State which cell type is depicted.
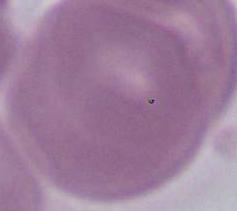
This is an erythrocyte.

Summary:
  - Modality: micrograph
  - Magnification: 1000x